Give a bounding box for every parasitised red blood cell, every trophozoite, every gametocyte, every leukocyte, and every artifact (platelet-like body, stain precipitate, or debris).
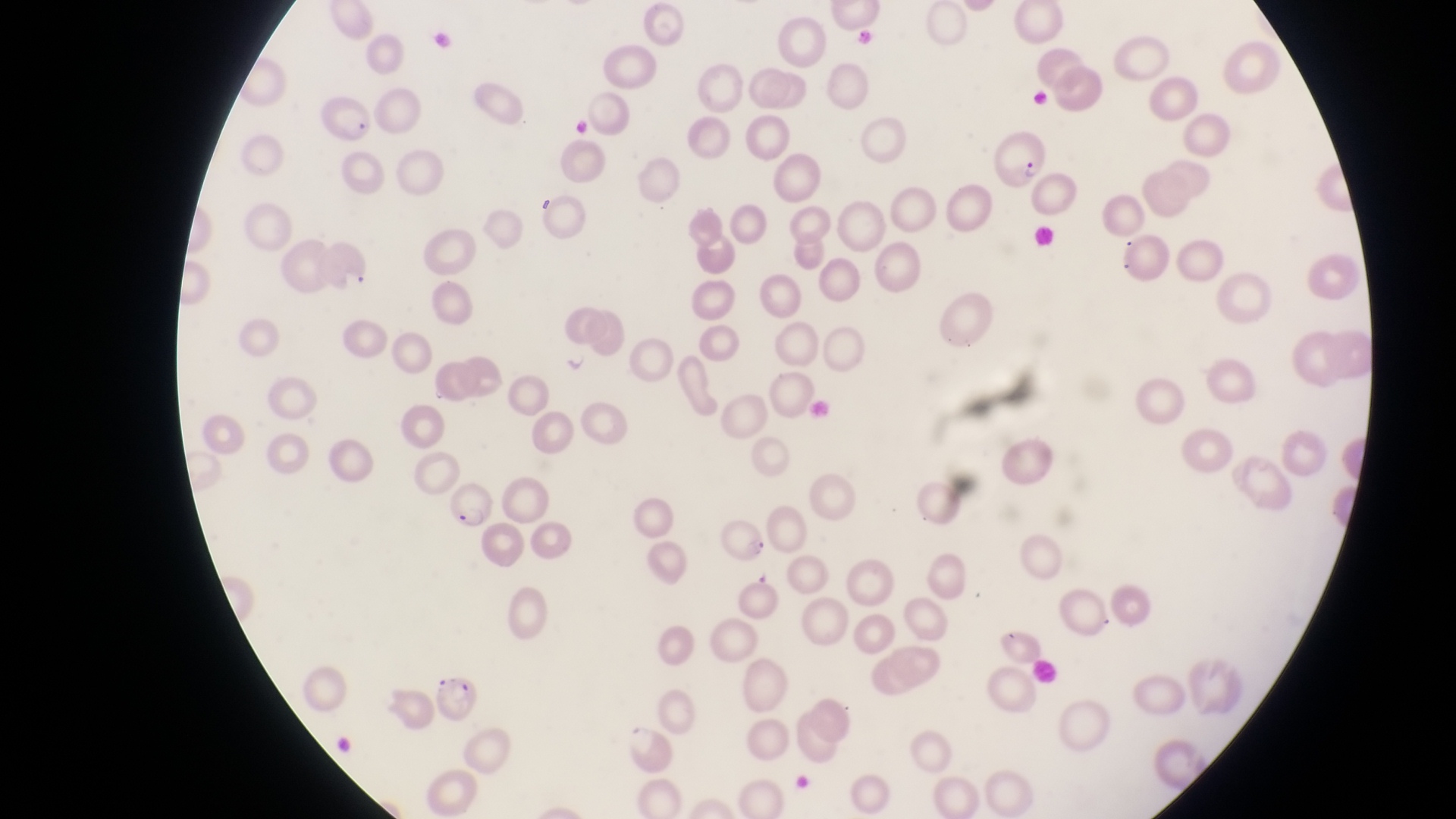

Approximate bounding boxes as (left, top, right, bottom) in pixels.
Parasitised red blood cells: (314, 96, 375, 146), (994, 126, 1052, 189), (444, 479, 493, 532), (435, 673, 482, 731).
Trophozoites: (557, 343, 596, 375).
No leukocytes observed.

Summary:
  - Field of view: single
  - Preparation: thin blood film
  - Country: Uganda
  - Magnification: 1000x
  - Capture: smartphone photograph through the eyepiece of an Olympus CX-23 microscope
  - Image size: 1456×819 pixels